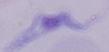

Micrograph. 1000x magnification. A trypanosome is shown.